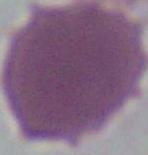
Summary:
  - Modality: micrograph
  - Identification: erythrocyte
  - Magnification: 1000x